Classify this cell by malaria status.
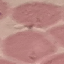

It is uninfected.

Giemsa stain. Photographed with a smartphone camera at the microscope eyepiece. Automatically extracted cell patch, resized to 64 × 64 pixels. Thin blood smear.